Classify this cell by malaria status.
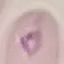
It is uninfected.

{
  "image_type": "cell patch, automatically extracted from a larger field of view and resized to 64 × 64 pixels",
  "capture": "smartphone through the microscope eyepiece",
  "stain": "Giemsa",
  "preparation": "thin blood smear"
}